Report the malaria status of this cell.
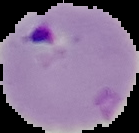
Parasitized.

Summary:
  - Image size: 139×133 pixels
  - Image type: cell region segmented out of the field of view; surrounding area masked to black
  - Preparation: thin blood smear